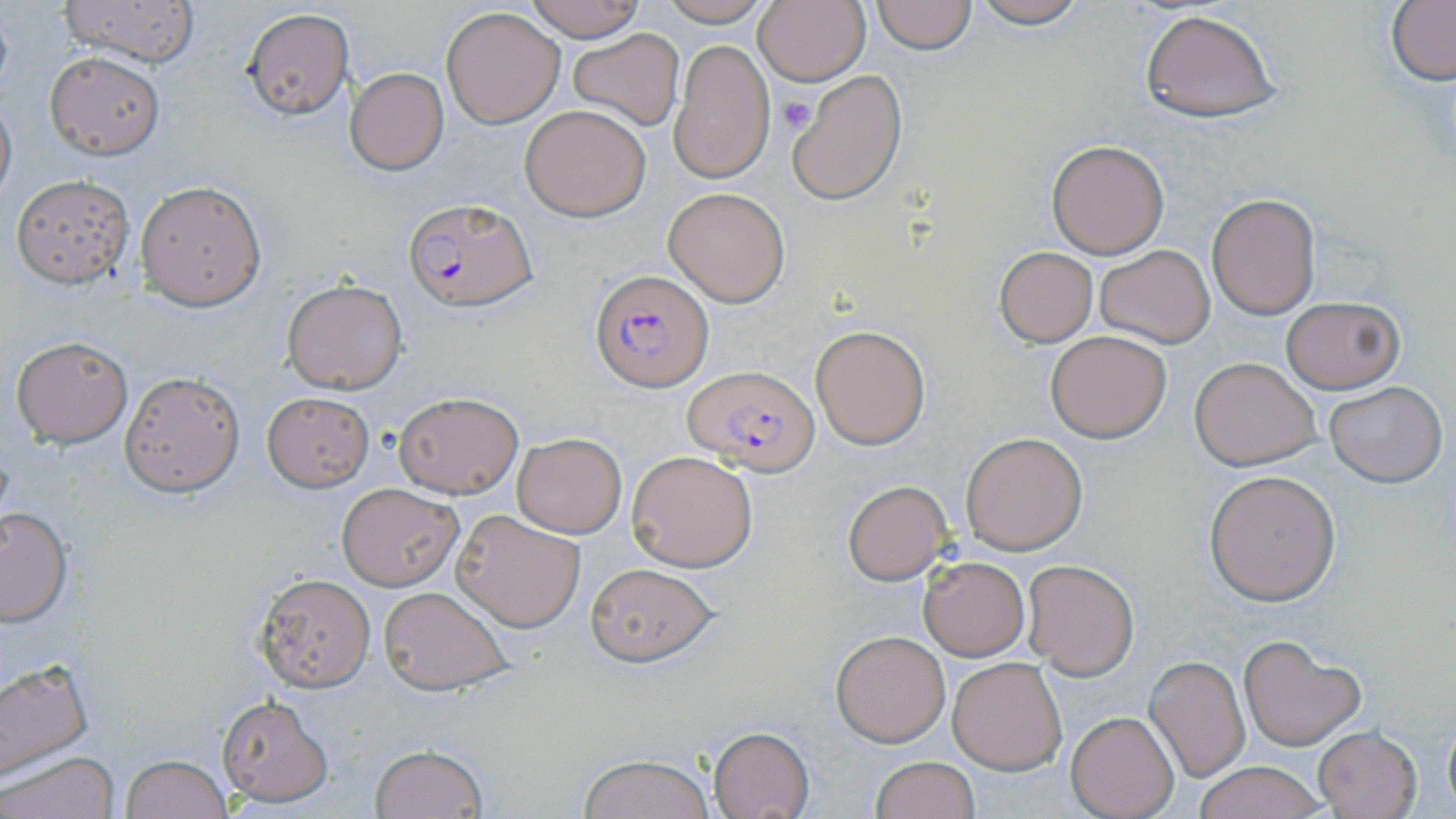
Approximate bounding boxes as (x1, y1, x2, y2) in pixels. Uninfected red blood cell locations: (60, 0, 202, 69), (524, 0, 647, 41), (656, 0, 777, 26), (753, 0, 869, 87), (870, 0, 976, 53), (965, 0, 1092, 28), (1386, 1, 1456, 85), (442, 6, 565, 127), (243, 8, 354, 120), (1136, 8, 1283, 123), (567, 29, 684, 132), (669, 37, 774, 185), (45, 52, 163, 158), (345, 69, 449, 174), (790, 69, 908, 204), (0, 90, 17, 207), (520, 103, 652, 221), (1046, 138, 1170, 259), (12, 175, 133, 287), (137, 181, 265, 310), (663, 188, 789, 307), (1206, 193, 1320, 320), (993, 246, 1099, 347), (1095, 246, 1215, 347), (282, 280, 407, 393), (1280, 296, 1404, 393), (812, 327, 930, 449), (1045, 330, 1172, 442), (11, 336, 133, 448), (1190, 356, 1319, 470), (119, 370, 244, 498), (1324, 382, 1447, 487), (393, 391, 525, 499), (261, 392, 373, 491), (960, 431, 1088, 556), (511, 432, 627, 537), (627, 450, 758, 573), (1204, 471, 1340, 605), (843, 480, 953, 584), (338, 484, 462, 591), (0, 507, 73, 627), (452, 509, 583, 631), (918, 557, 1030, 662), (1022, 560, 1138, 679), (584, 564, 716, 666), (255, 573, 375, 692), (378, 586, 511, 696), (829, 629, 949, 746), (1239, 634, 1365, 749), (1145, 654, 1250, 783), (948, 656, 1067, 775), (0, 658, 95, 785), (217, 695, 333, 806), (1066, 711, 1178, 819), (1442, 711, 1455, 814), (707, 726, 816, 819), (1313, 726, 1422, 818), (369, 744, 488, 818), (1, 749, 120, 819), (120, 753, 232, 819), (577, 754, 719, 819), (868, 755, 979, 819), (1192, 761, 1326, 819). Platelet locations: (775, 95, 816, 136). Plasmodium falciparum-infected red blood cell locations: (405, 199, 537, 310), (591, 269, 714, 390), (684, 366, 819, 475). Slide-level diagnosis: Plasmodium falciparum. Thin blood film. Light microscopy. May-Grünwald-Giemsa stain. One field of a larger specimen. Captured at 1000x magnification. Image is 1456×819 pixels.